Assess the morphology of the erythrocytes.
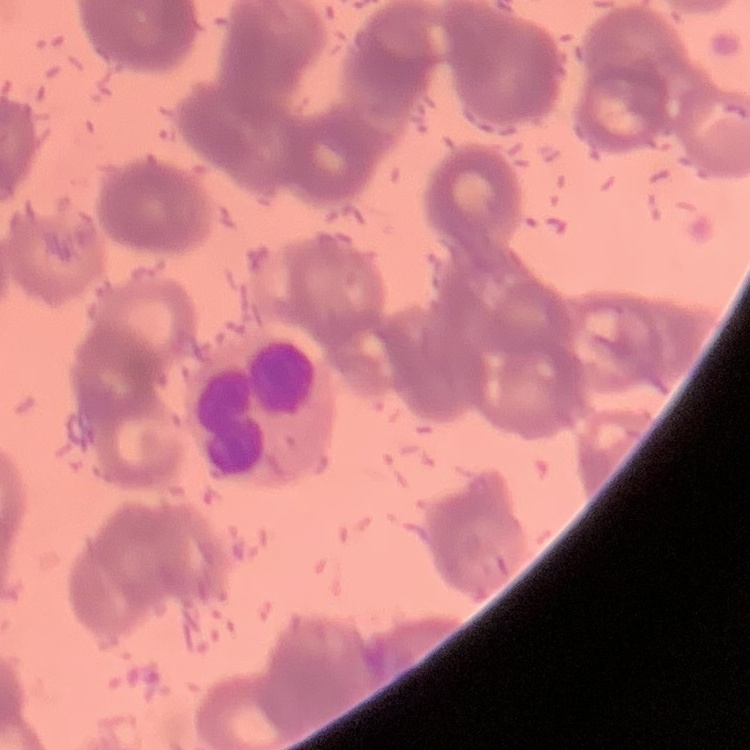
Rouleaux formation.

Field's or Giemsa stain. One tile cut from a larger photomicrograph. Thin peripheral smear.